Identify the cell.
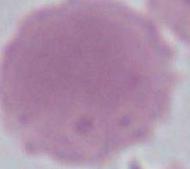
This is an erythrocyte.

Captured at 1000x magnification. Micrograph.